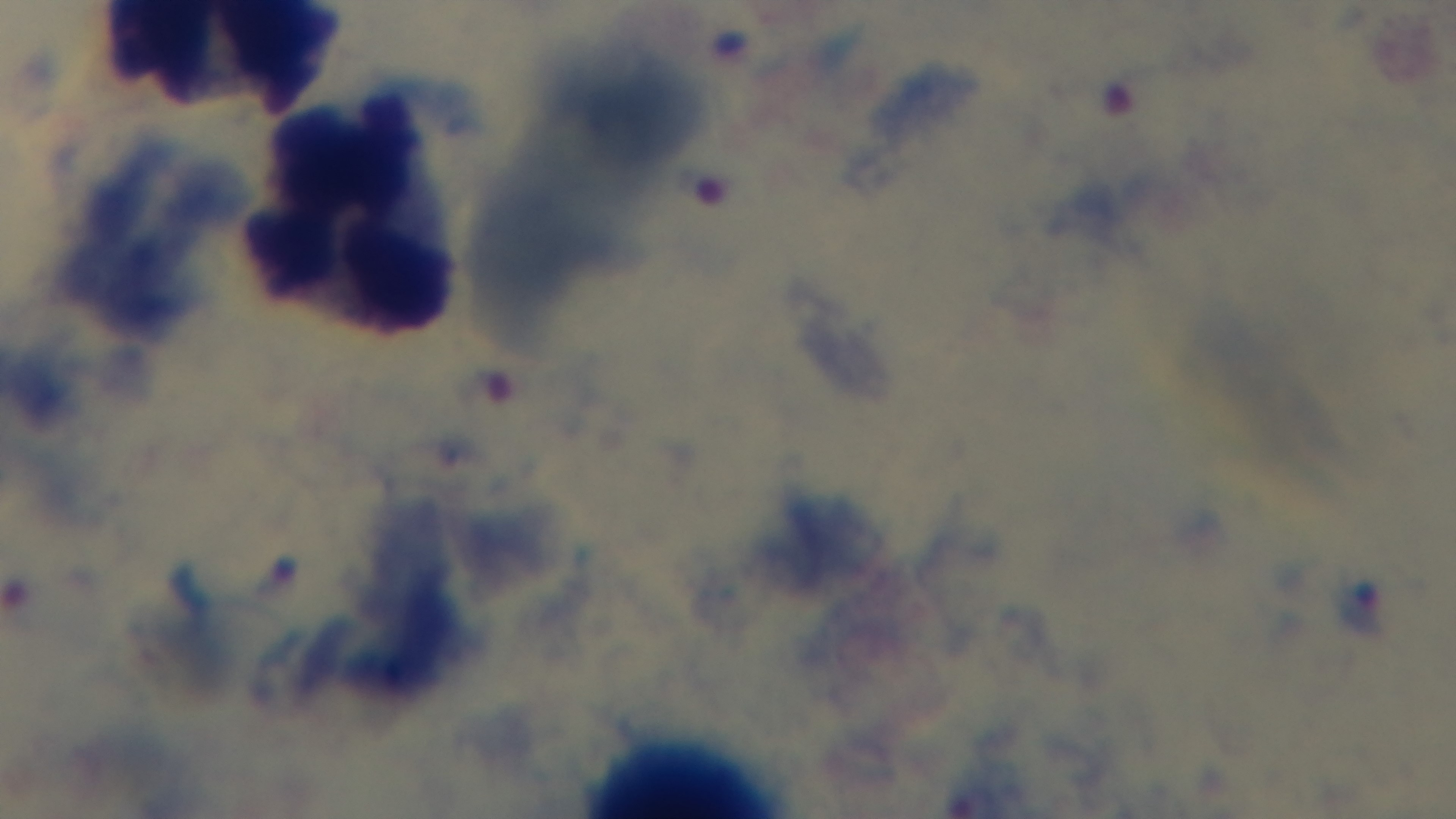
Malaria status: infected. Single field of view. Photomicrograph. Giemsa-stained. Oil-immersion objective, 100x. Mounted 4K digital camera. Preparation: thick smear.